State which parasite is depicted.
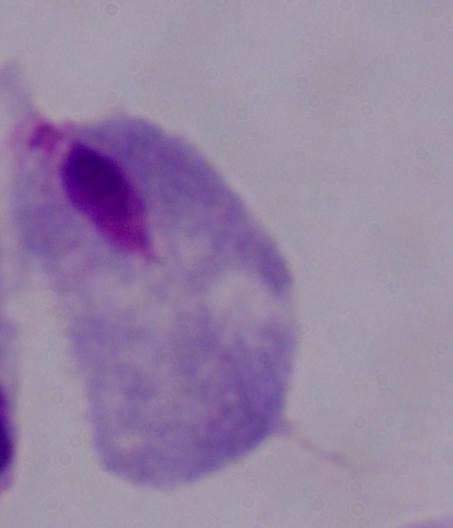

A trichomonad.

{
  "modality": "photomicrograph",
  "magnification": "1000x"
}